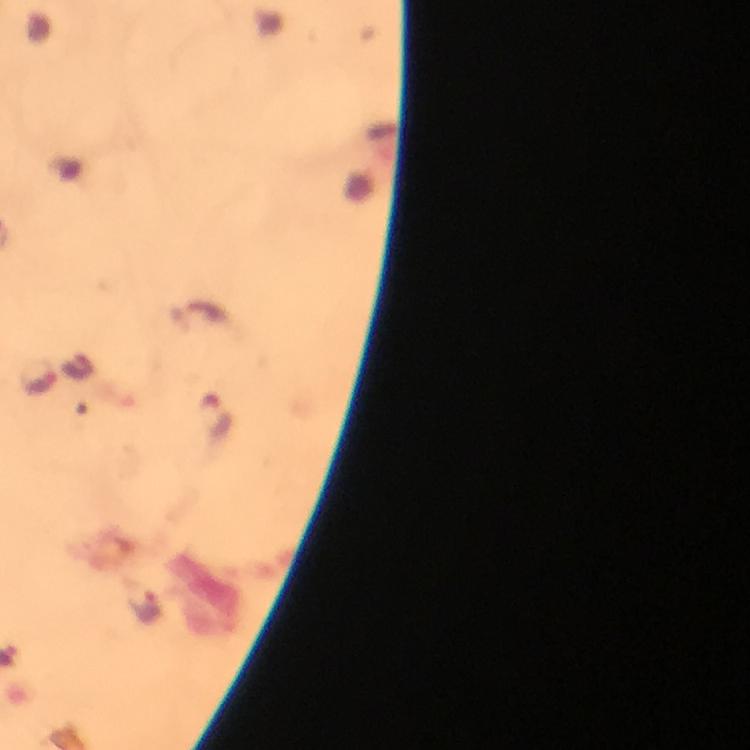

{
  "cropped_from": "one field of view",
  "preparation": "thick smear",
  "context": "from a malaria diagnostic workup",
  "immersion_oil": "used",
  "plasmodium_parasite_locations": "approximate centers as {x, y} in pixels: {37, 374}, {216, 414}, {146, 607}",
  "stain": "Giemsa",
  "magnification": "100x",
  "capture": "smartphone camera through the microscope",
  "image_size": "750×750 pixels"
}